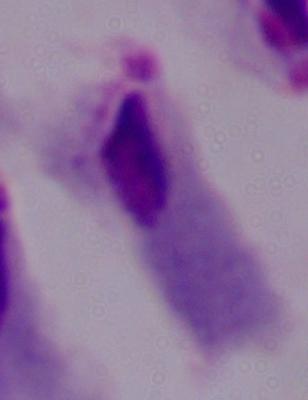

Summary:
  - Modality: photomicrograph
  - Magnification: 1000x
  - Identification: trichomonad